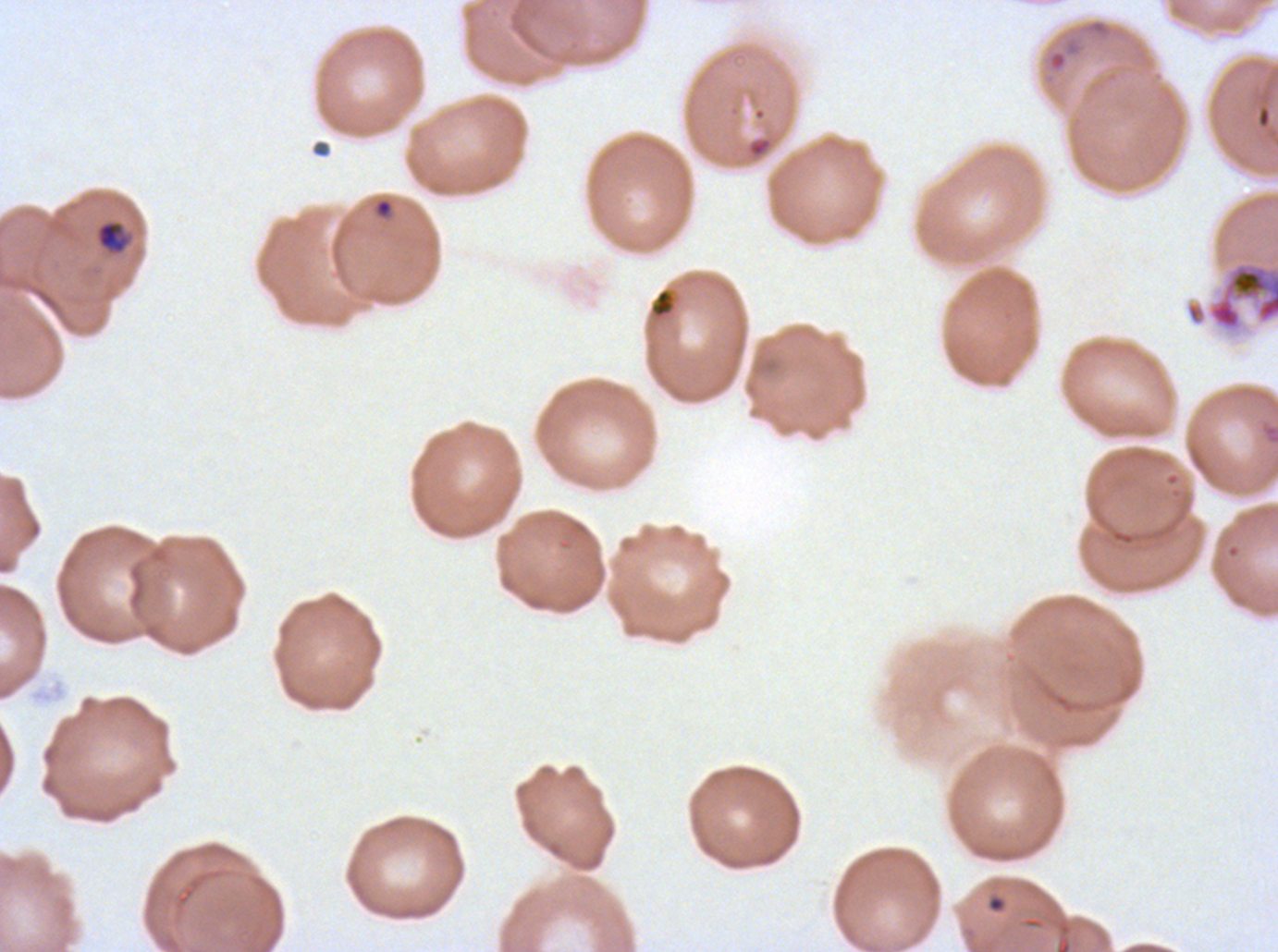
notation = approximate bounding boxes as {x1, y1, x2, y2} in pixels
debris locations = {1044, 33, 1085, 75}, {648, 287, 677, 320}
early schizont locations = {1206, 260, 1277, 334}
ring locations = {374, 197, 394, 219}, {986, 893, 1007, 914}
late-ring/early-trophozoite locations = {95, 220, 129, 254}
field of view = sub-image separated from a larger composite
specimen = Plasmodium falciparum cultured ex vivo for 24 to 48 hours, from a patient in The Gambia
stain = Giemsa
life-cycle stages observed = ring, late-ring/early-trophozoite, early schizont
preparation = thin blood smear
image size = 1278×952 pixels